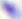
{
  "identification": "Toxoplasma gondii",
  "magnification": "400x",
  "modality": "photomicrograph"
}